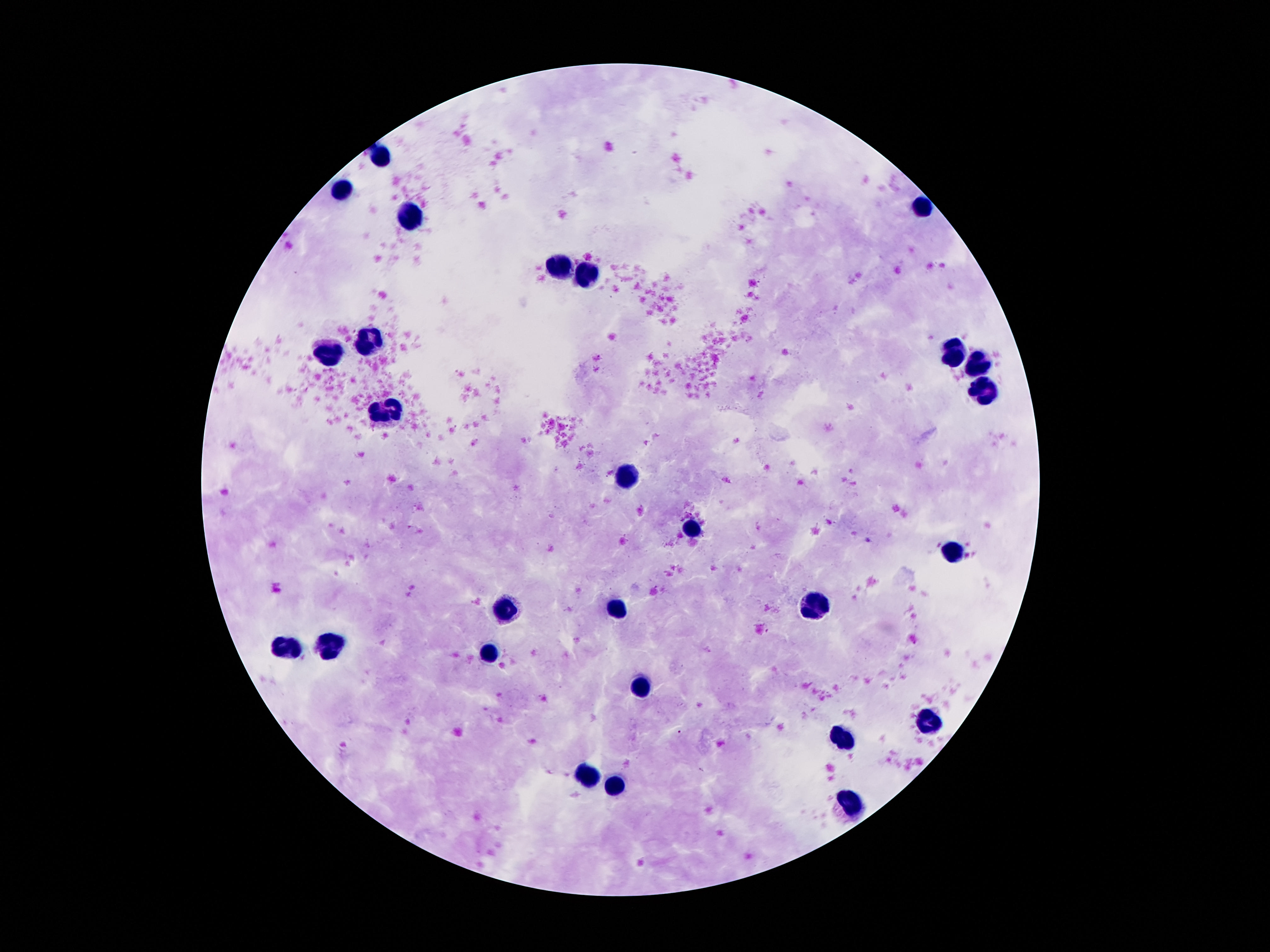 Approximate centers as [x, y] in pixels. Leukocyte locations: [379, 156], [341, 189], [922, 208], [407, 216], [559, 268], [589, 274], [369, 344], [951, 349], [328, 354], [978, 364], [983, 391], [386, 414], [626, 475], [689, 529], [950, 554], [815, 602], [617, 610], [503, 611], [337, 646], [293, 648], [491, 653], [640, 687], [929, 721], [846, 737], [589, 775], [614, 786], [852, 803]. One field from this slide. 100x magnification. Thick peripheral-blood smear. Giemsa-stained preparation. Image is 1270×952 pixels. Patient malaria status: negative. Photographed through the microscope eyepiece with a smartphone camera.